Report the malaria status of this cell.
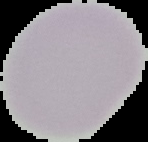

Uninfected.

The area outside the segmented cell region is set to black. From a thin blood smear. Image is 148×142 pixels.